Give the extent of all uninfected red blood cells.
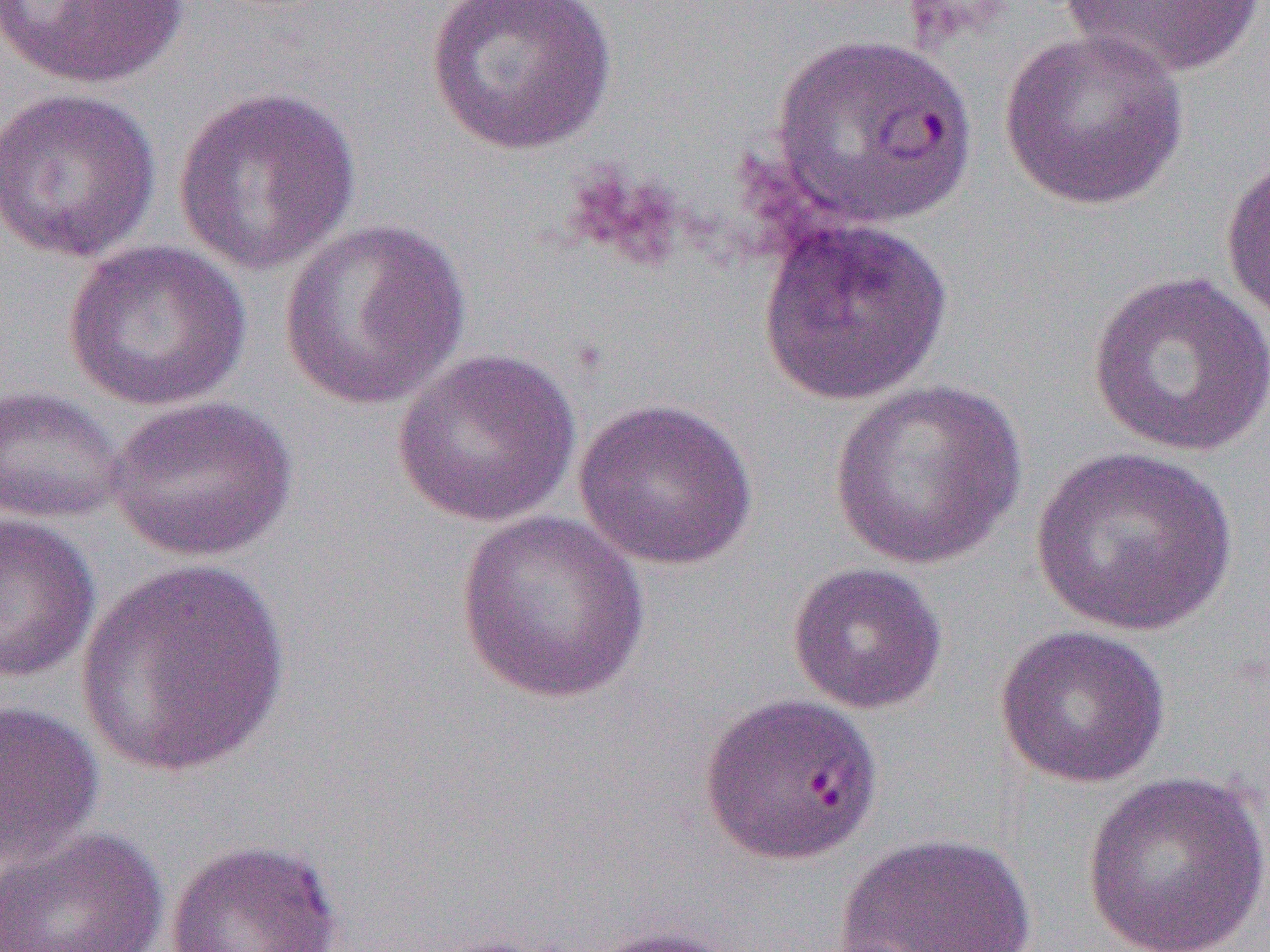
Approximate bounding boxes as (x1, y1, x2, y2) in pixels.
Uninfected red blood cells: (425, 0, 617, 156), (1059, 0, 1265, 80), (2, 1, 189, 89), (998, 28, 1191, 211), (770, 32, 977, 231), (0, 86, 163, 263), (172, 86, 362, 276), (1219, 149, 1270, 325), (756, 216, 953, 407), (277, 217, 472, 410), (61, 239, 250, 413), (1087, 270, 1270, 458), (392, 347, 582, 527), (828, 378, 1027, 570), (0, 385, 127, 524), (104, 395, 297, 563), (572, 398, 760, 571), (1028, 445, 1240, 639), (455, 510, 651, 705), (0, 511, 100, 685), (75, 558, 294, 781), (786, 561, 948, 714), (994, 624, 1171, 789), (699, 692, 884, 865), (0, 699, 104, 868), (1079, 771, 1270, 952), (0, 826, 169, 952), (833, 831, 1037, 952), (164, 838, 344, 951), (576, 925, 747, 952), (417, 932, 571, 952).

Summary:
  - Slide-level diagnosis: Plasmodium falciparum
  - Image size: 1270×952 pixels
  - Magnification: 1000x
  - Modality: light microscopy
  - Field of view: one of a larger specimen
  - Preparation: thin blood smear